Give the position of every Plasmodium parasite.
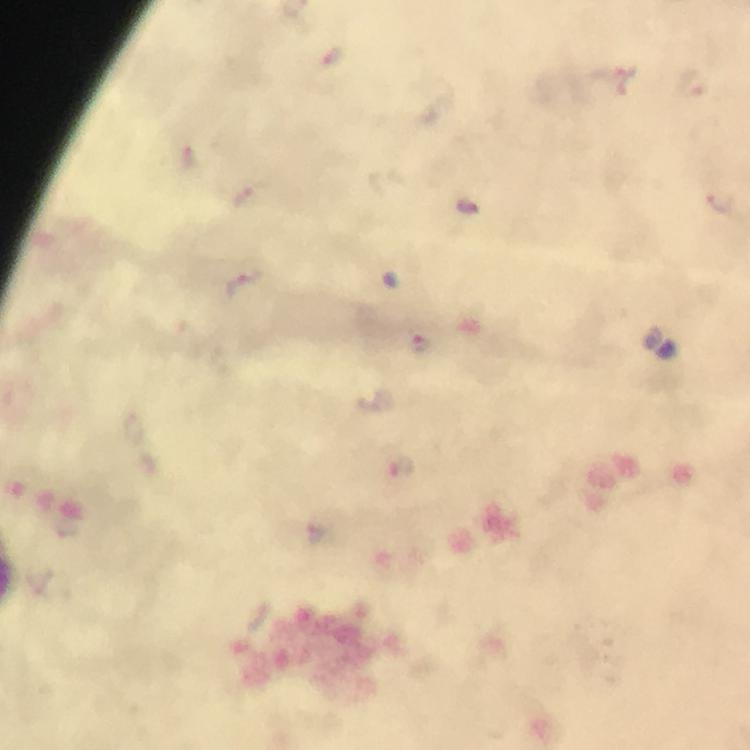
Approximate centers as [x, y] in pixels.
Plasmodium parasites: [333, 55], [614, 79], [192, 157], [725, 203], [469, 206], [241, 285], [421, 343], [403, 467].

{
  "preparation": "thick blood smear",
  "context": "from a diagnostic examination for malaria",
  "capture": "smartphone camera through the microscope",
  "magnification": "100x",
  "image_size": "750×750 pixels",
  "cropped_from": "one field of view",
  "stain": "Giemsa",
  "immersion_oil": "used"
}